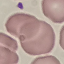
Summary:
  - Malaria status: uninfected
  - Capture: smartphone through the microscope eyepiece
  - Image type: cell patch, automatically extracted from a larger field of view and resized to 64 × 64 pixels
  - Preparation: thin blood smear
  - Stain: Giemsa